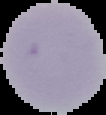

{
  "result": "no Plasmodium parasites detected",
  "image_size": "106×115 pixels",
  "preparation": "thin blood film",
  "image_type": "segmented cell region on a black background"
}